Report the malaria status of this cell.
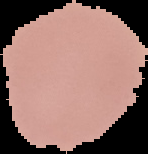

It is uninfected.

{
  "preparation": "thin blood film",
  "image_size": "148×154 pixels",
  "image_type": "segmented cell region with the area outside set to black"
}